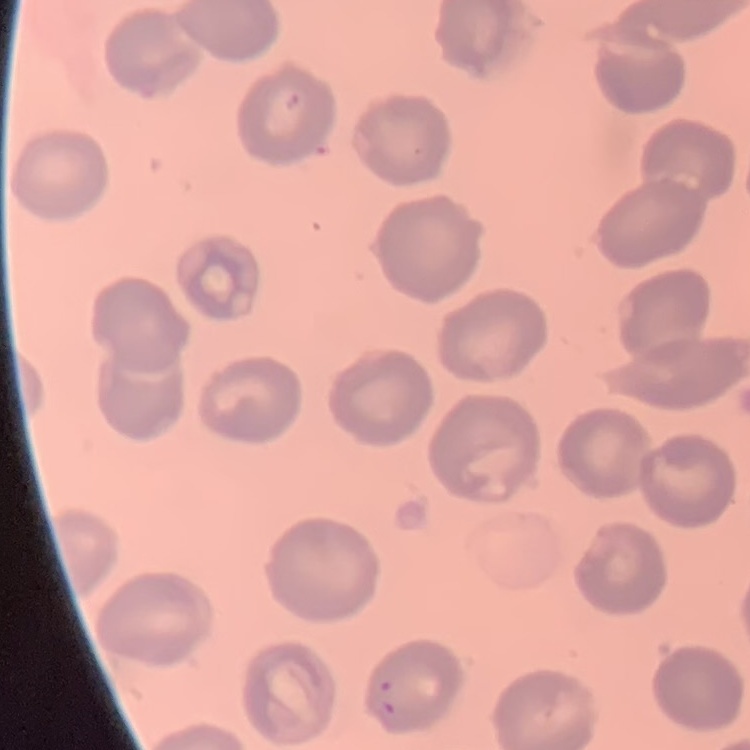

The red blood cells exhibit no rouleaux formation. Square crop of a larger photomicrograph. Thin peripheral smear. Stained with either Field's or Giemsa.